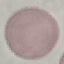

Summary:
  - Malaria status: uninfected
  - Capture: smartphone camera at the microscope eyepiece
  - Image type: cell patch, automatically extracted from a larger field of view and resized to 64 × 64 pixels
  - Stain: Giemsa
  - Preparation: thin blood film